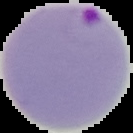
result = Plasmodium parasites identified
image type = cell region segmented out of the field of view; surrounding area masked to black
preparation = thin blood smear
image size = 133×133 pixels